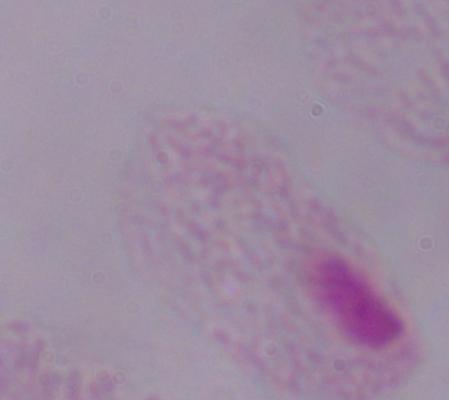

Summary:
  - Magnification: 1000x
  - Modality: micrograph
  - Identification: trichomonad